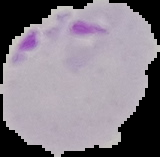
image size = 160×157 pixels
image type = segmented cell region on a black background
result = Plasmodium parasites detected
preparation = thin blood smear